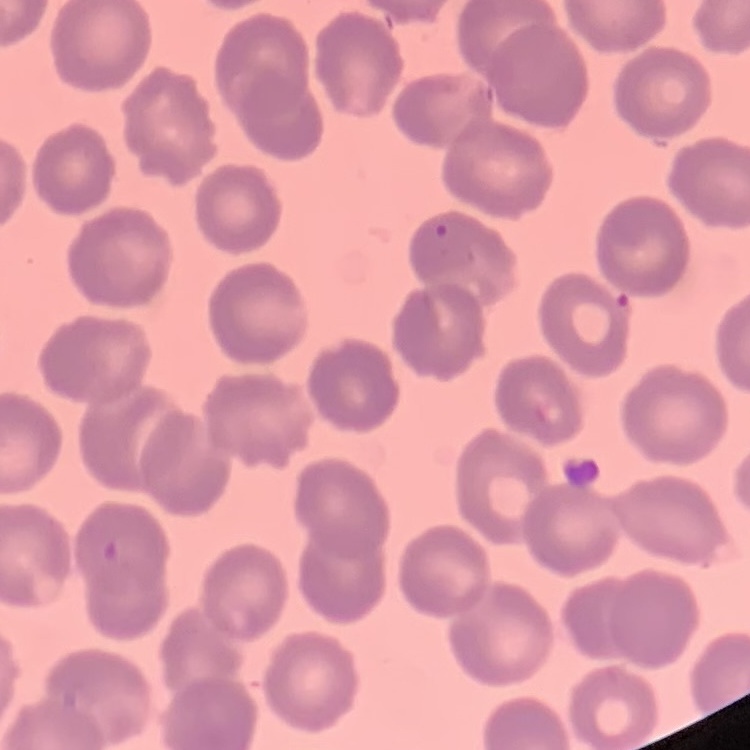
red blood cell morphology = no rouleaux formation
preparation = thin blood smear
image type = square crop of a larger photomicrograph
stain = Field's or Giemsa